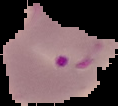
From a thin blood smear. Segmented cell region on a black background. Result: Plasmodium parasites detected. Image is 118×106 pixels.